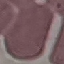

Summary:
  - Result: no malaria parasites seen
  - Capture: smartphone camera at the microscope eyepiece
  - Preparation: thin smear
  - Stain: Giemsa
  - Image type: automatically extracted cell patch, resized to 64 × 64 pixels